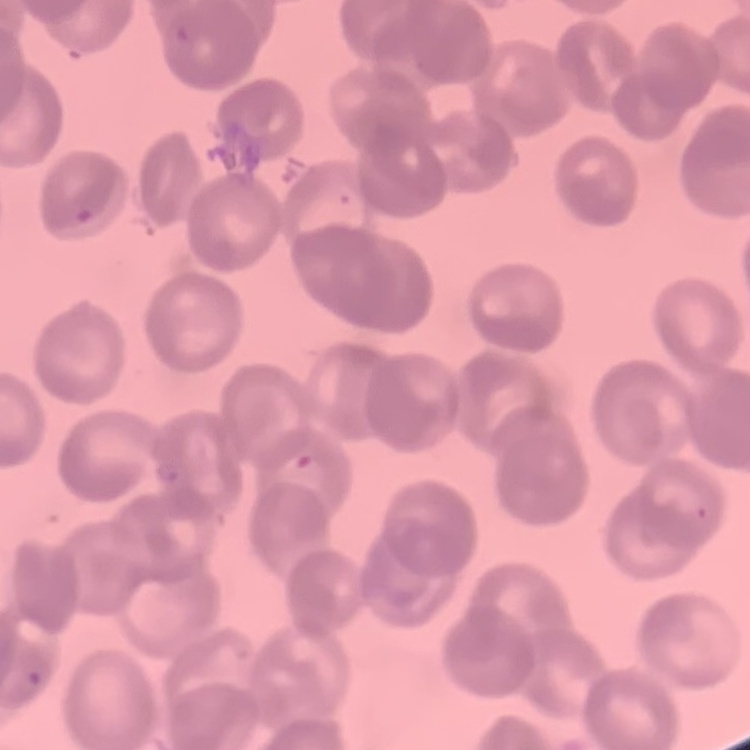
red blood cell morphology = rouleaux formation
image type = one tile cut from a larger photomicrograph
stain = Field's or Giemsa
preparation = thin peripheral smear